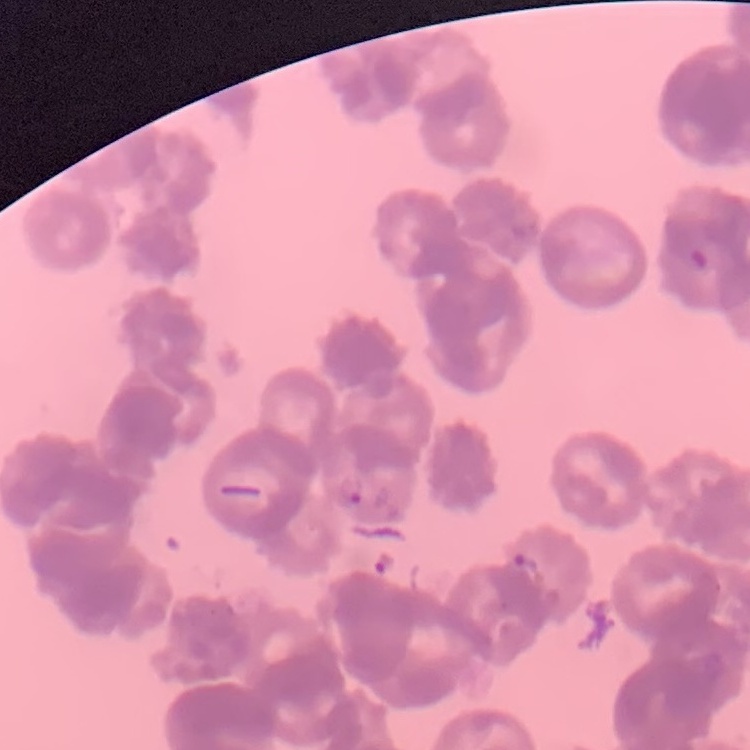 The erythrocytes exhibit rouleaux formation. Thin blood film. One tile cut from a larger photomicrograph. Field's or Giemsa stain.